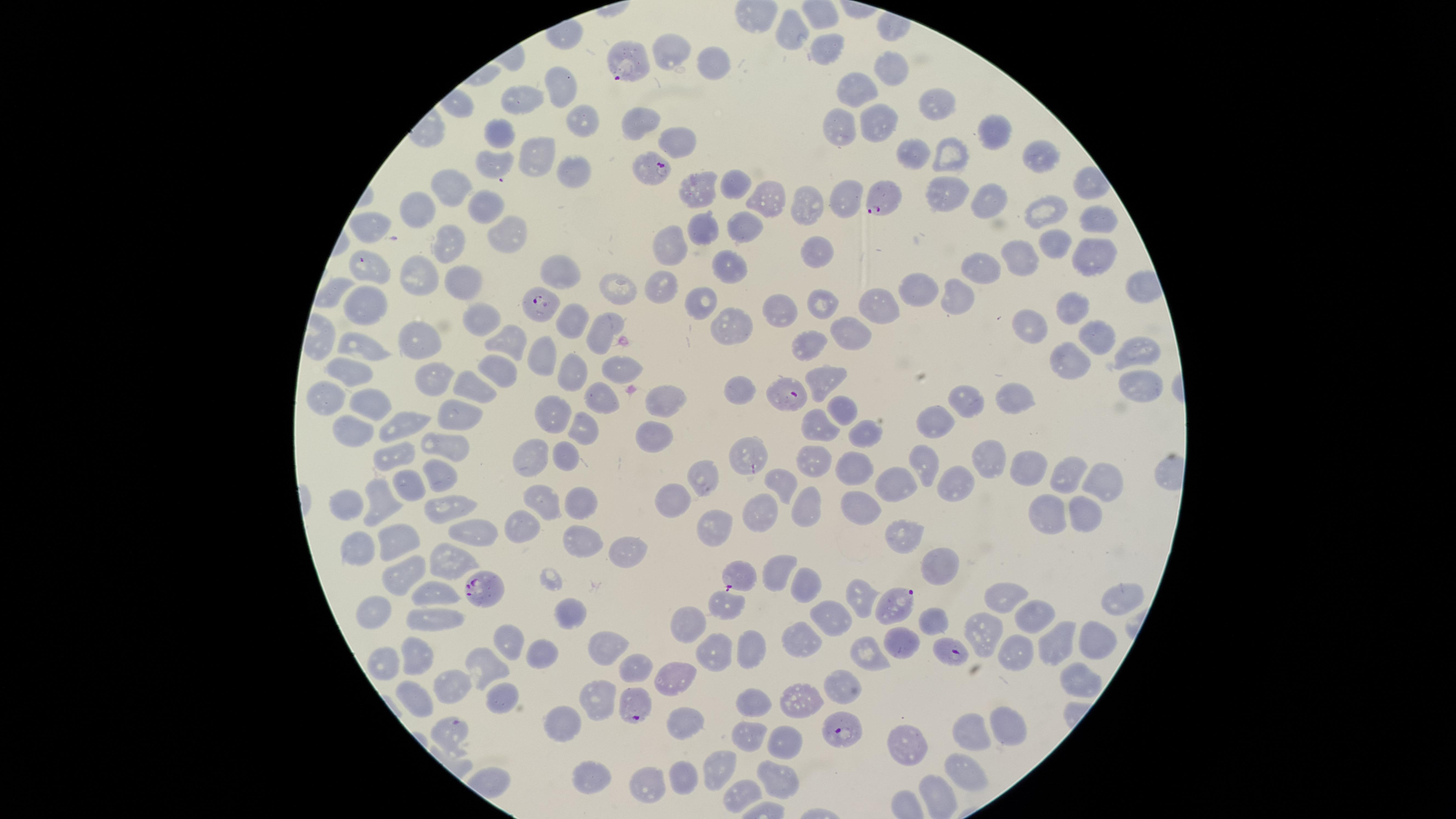
{
  "image_size": "1456×819 pixels",
  "preparation": "thin blood film",
  "presence": "malaria parasites seen",
  "species": "Plasmodium falciparum",
  "field_of_view": "single",
  "uninfected_red_blood_cells": "approximate marker points as (x, y) in pixels: (796, 33), (834, 48), (670, 51), (708, 63), (887, 68), (560, 85), (856, 87), (528, 101), (929, 101), (584, 116), (874, 119), (639, 120), (836, 129), (992, 131), (499, 134), (676, 141), (950, 148), (908, 153), (1035, 153), (534, 154), (491, 166), (570, 176), (737, 179), (694, 183), (445, 187), (942, 192), (766, 199), (993, 199), (841, 202), (482, 207), (803, 207), (1044, 207), (418, 211), (1097, 215), (367, 227), (742, 228), (704, 230), (510, 235), (443, 241), (1054, 241), (674, 248), (817, 253), (1022, 253), (1085, 256), (371, 261), (419, 264), (977, 267), (727, 268), (466, 277), (924, 283), (618, 285), (952, 293), (659, 294), (872, 296), (824, 302), (360, 303), (705, 303), (781, 307), (1063, 312), (471, 317), (1032, 320), (571, 322), (727, 322), (850, 331), (606, 332), (356, 335), (1097, 340), (412, 341), (505, 341), (807, 346), (544, 353), (1067, 357), (1131, 359), (349, 361), (504, 371), (576, 373), (624, 374), (827, 374), (428, 377), (1138, 384), (462, 387), (738, 391), (668, 396), (977, 396), (1013, 396), (324, 398), (598, 402), (363, 406), (841, 407), (454, 410), (555, 413), (933, 419), (398, 424), (819, 424), (589, 429), (354, 430), (862, 431), (656, 432), (450, 441), (533, 455), (567, 455), (748, 455), (992, 455), (816, 456), (395, 457), (854, 467), (924, 467), (1031, 470), (1059, 471), (432, 473), (702, 474), (782, 483), (895, 483), (954, 486), (1102, 486), (408, 490), (541, 491), (346, 499), (672, 499), (382, 501), (436, 503), (800, 503), (575, 504), (861, 505), (763, 513), (1046, 515), (1074, 515), (522, 525), (712, 526), (471, 531), (402, 537), (899, 537), (571, 541), (356, 548), (624, 555), (448, 557), (932, 568), (771, 569), (397, 576), (802, 576), (1005, 592), (431, 595), (860, 595), (720, 605), (1116, 605), (380, 610), (569, 611), (832, 612), (1035, 613), (437, 614), (930, 621), (685, 622), (981, 631), (801, 638), (900, 641), (505, 642), (1053, 642), (610, 644), (745, 645), (1088, 645), (710, 648), (538, 651), (1012, 651), (866, 654), (416, 657), (389, 663), (487, 663), (632, 664), (1079, 672), (674, 673), (844, 684), (456, 687), (418, 697), (501, 698), (594, 704), (751, 705), (801, 705), (677, 718), (1013, 722), (565, 725), (966, 730), (442, 735), (749, 740), (783, 741), (905, 748), (717, 761), (960, 767), (683, 773), (589, 775), (776, 775), (642, 784), (939, 791), (730, 793)",
  "capture": "smartphone photograph through the microscope eyepiece",
  "parasitized_red_blood_cells": "approximate marker points as (x, y) in pixels: (630, 63), (653, 172), (887, 199), (539, 304), (785, 390), (736, 575), (477, 586), (891, 601), (959, 652), (630, 703), (839, 728)",
  "visible_region": "circular",
  "stain": "Giemsa"
}